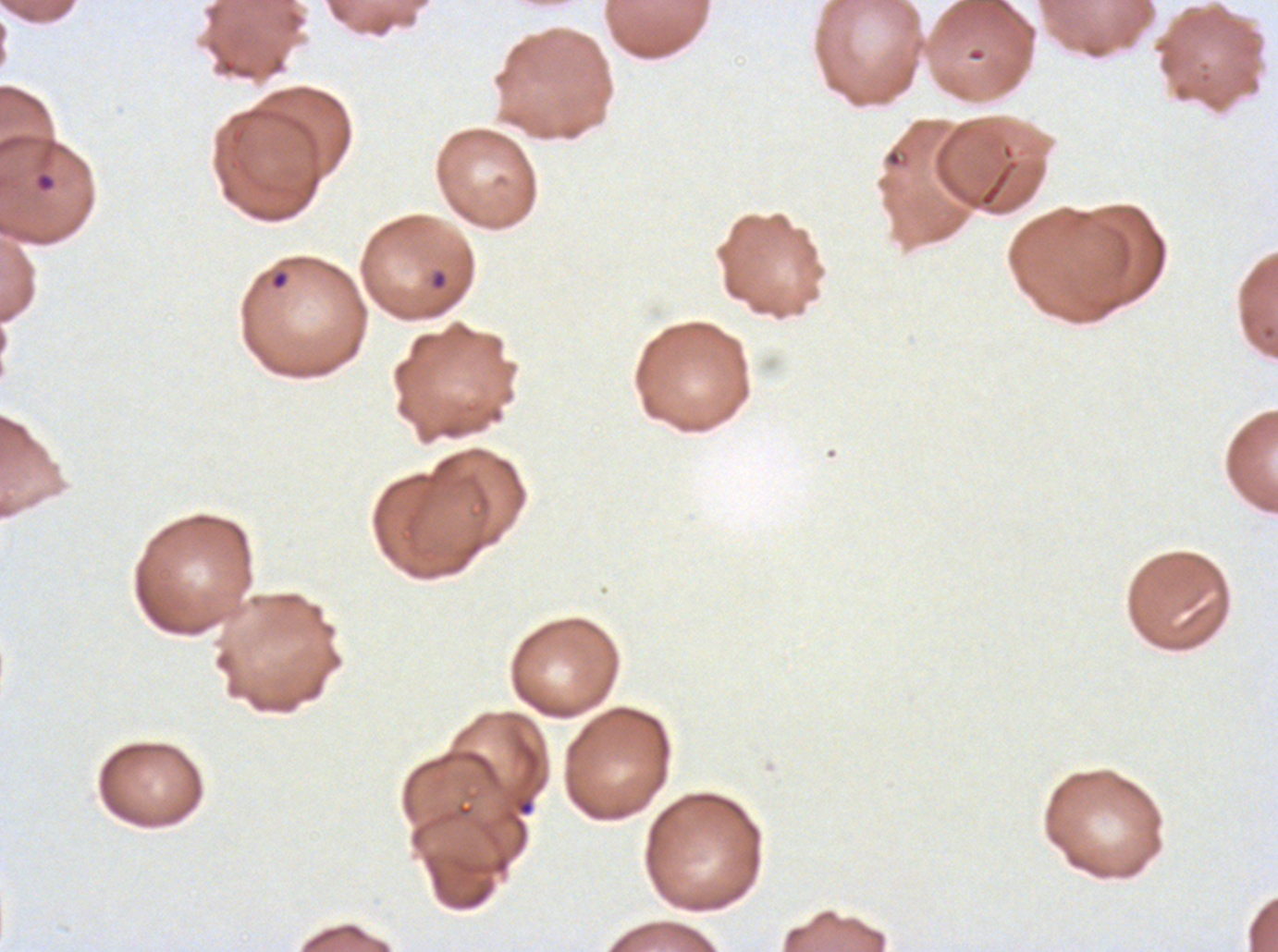 Approximate bounding boxes as [x1, y1, x2, y2] in pixels. Debris locations: [513, 796, 535, 817]. Ring locations: [33, 170, 57, 193], [428, 268, 449, 291], [269, 269, 290, 291]. One sub-image of a larger composite. Giemsa stain. Plasmodium falciparum from a patient in The Gambia, cultured ex vivo for 24 to 48 hours. Image is 1278×952 pixels. Thin blood smear.